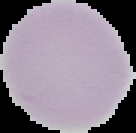 From a thin blood film. Image is 136×133 pixels. Segmented cell region on a black background. Malaria status: uninfected.